Name the parasite shown.
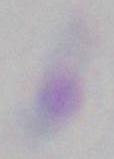

This is Toxoplasma gondii.

1000x magnification. Photomicrograph.